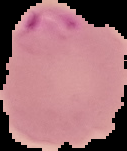
image size = 127×151 pixels
preparation = thin blood smear
image type = segmented cell region with the area outside set to black
result = Plasmodium parasites detected